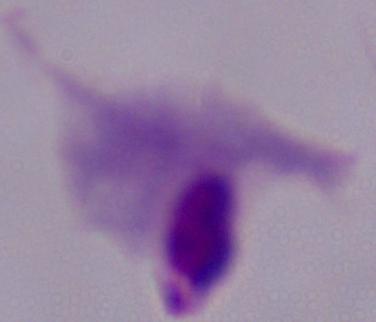

Captured at 1000x magnification. A trichomonad is seen. Photomicrograph.